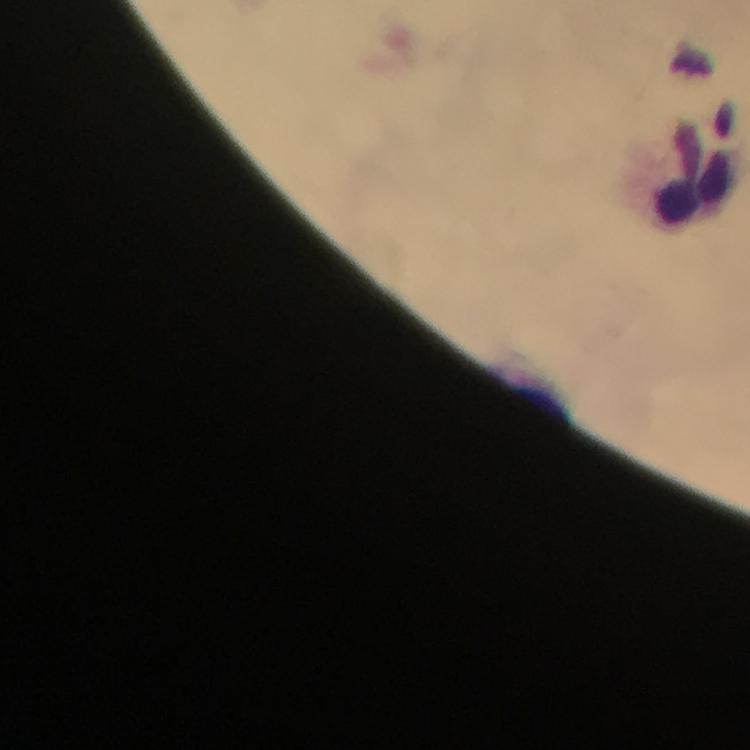

malaria parasites = none detected
context = from a diagnostic examination for malaria
capture = smartphone mounted on the microscope
preparation = thick blood film
image size = 750×750 pixels
cropped from = one field of view
leukocyte locations = approximate object centers, in pixels from the top-left corner: (x=697, y=165)
immersion oil = applied
magnification = 100x
stain = Giemsa